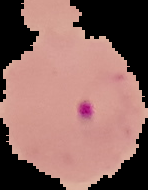

Image is 148×190 pixels. From a thin blood film. Result: Plasmodium parasites detected. Segmented cell region on a black background.